Locate every white blood cell.
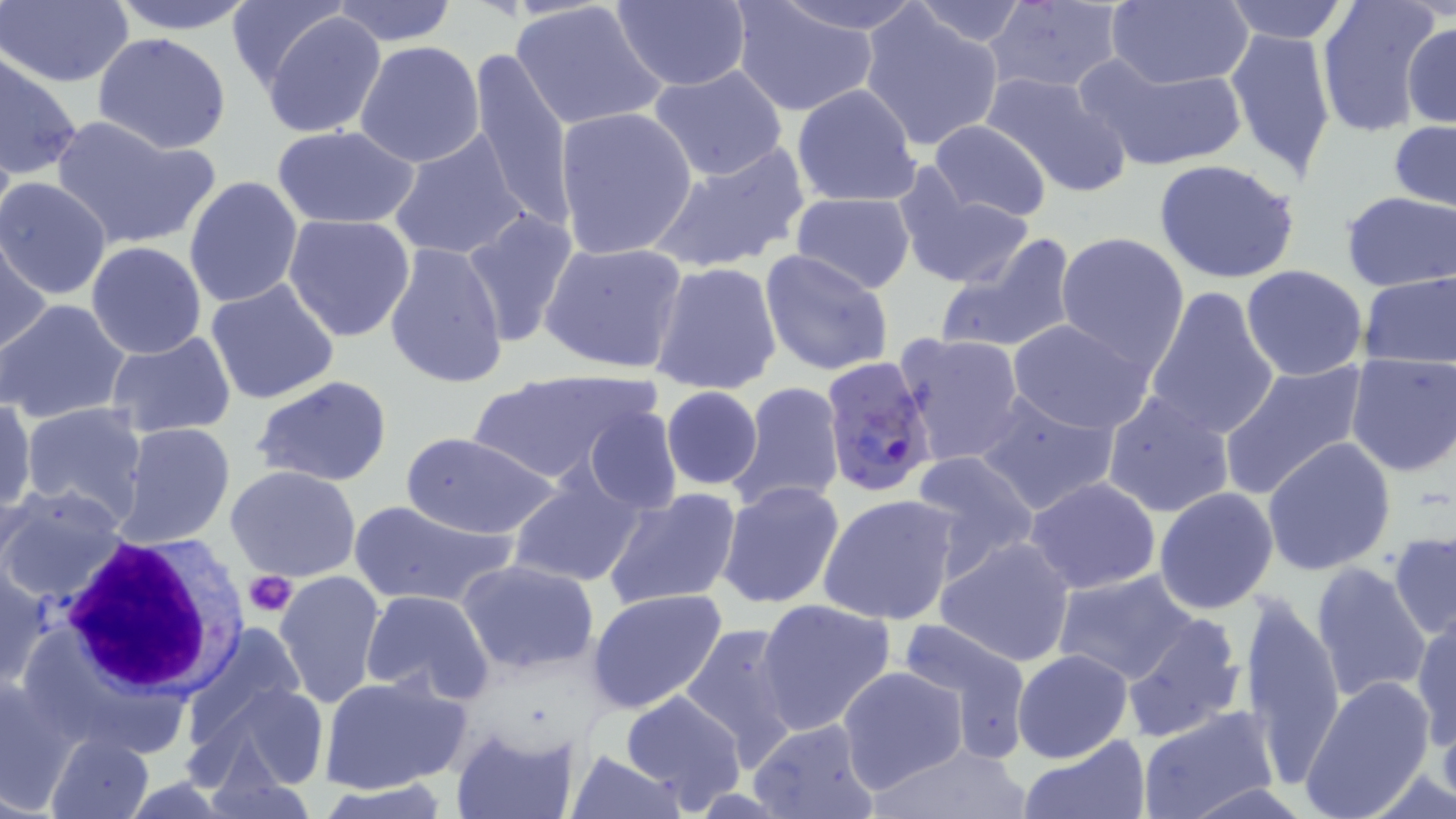

Approximate bounding boxes as (x1, y1, x2, y2) in pixels.
White blood cells: (54, 532, 244, 704).

Summary:
  - Platelet locations: (243, 569, 296, 618)
  - Plasmodium falciparum-infected red blood cell locations: (822, 356, 939, 496)
  - Uninfected red blood cell locations: (1, 0, 132, 87), (103, 0, 262, 35), (728, 0, 882, 119), (769, 0, 932, 36), (1314, 0, 1442, 138), (329, 1, 458, 47), (510, 1, 666, 132), (611, 1, 752, 90), (904, 1, 1035, 47), (1103, 1, 1253, 89), (1220, 1, 1350, 43), (227, 2, 353, 90), (980, 3, 1131, 94), (857, 6, 1007, 153), (259, 10, 389, 140), (1403, 20, 1455, 131), (1224, 27, 1337, 184), (93, 32, 232, 154), (354, 40, 486, 169), (468, 47, 576, 232), (1076, 50, 1249, 174), (0, 53, 84, 181), (645, 62, 792, 184), (980, 70, 1135, 200), (792, 84, 921, 207), (554, 106, 697, 258), (50, 115, 220, 251), (1387, 118, 1456, 217), (927, 119, 1053, 221), (272, 126, 419, 229), (387, 128, 531, 264), (648, 139, 812, 274), (1153, 159, 1301, 284), (895, 172, 1037, 294), (183, 176, 305, 307), (0, 177, 115, 300), (1339, 191, 1456, 292), (791, 192, 916, 294), (460, 207, 579, 346), (284, 213, 417, 342), (1054, 231, 1189, 373), (0, 235, 52, 355), (938, 236, 1079, 357), (85, 240, 208, 359), (385, 241, 509, 389), (540, 241, 688, 376), (759, 249, 894, 378), (650, 261, 784, 396), (1240, 265, 1370, 382), (1358, 270, 1455, 371), (204, 277, 339, 405), (1143, 283, 1280, 444), (0, 299, 131, 424), (1007, 318, 1154, 433), (105, 329, 236, 439), (896, 332, 1027, 467), (1345, 353, 1456, 479), (1219, 359, 1368, 500), (469, 369, 657, 487), (252, 376, 392, 488), (729, 380, 846, 512), (661, 386, 763, 492), (974, 388, 1121, 517), (1101, 390, 1238, 520), (0, 397, 35, 515), (18, 402, 150, 526), (583, 406, 681, 513), (116, 423, 236, 548), (402, 430, 561, 540), (1263, 437, 1396, 577), (909, 450, 1040, 580), (226, 464, 363, 583), (507, 468, 645, 589), (1025, 476, 1162, 595), (717, 481, 845, 610), (0, 484, 129, 606), (488, 484, 629, 660), (1152, 487, 1279, 614), (602, 488, 744, 611), (817, 493, 962, 626), (346, 498, 513, 608), (1389, 531, 1456, 641), (932, 534, 1079, 668), (0, 559, 51, 690), (458, 559, 601, 674), (1311, 561, 1433, 704), (274, 569, 387, 709), (1050, 571, 1200, 686), (1237, 585, 1346, 786), (585, 588, 731, 716), (360, 590, 494, 707), (756, 597, 897, 737), (1119, 613, 1247, 744), (1412, 613, 1455, 752), (896, 618, 1036, 764), (678, 621, 806, 771), (182, 623, 307, 748), (1012, 648, 1134, 763), (837, 665, 969, 794), (318, 672, 471, 794), (0, 676, 77, 810), (1299, 676, 1436, 819), (205, 680, 332, 794), (620, 691, 748, 810), (1136, 705, 1282, 819), (745, 718, 880, 819), (449, 725, 580, 819), (46, 731, 155, 819), (1018, 737, 1149, 819), (865, 742, 1036, 817), (569, 746, 688, 819), (315, 782, 453, 818)
  - Slide-level diagnosis: Plasmodium falciparum
  - Field of view: single
  - Stain: May-Grünwald-Giemsa
  - Modality: optical microscopy
  - Preparation: thin blood film
  - Image size: 1456×819 pixels
  - Magnification: 1000x